State which parasite is depicted.
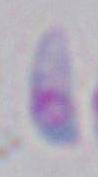

Toxoplasma gondii.

1000x magnification. Micrograph.